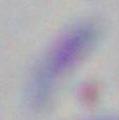
Captured at 1000x magnification. Micrograph. Toxoplasma gondii is seen.